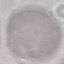

Malaria status: uninfected. Automatically extracted cell patch, resized to 64 × 64 pixels. Thin blood smear. Photographed with a smartphone camera at the microscope eyepiece. Giemsa-stained preparation.